Report the malaria status of this cell.
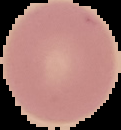

It is uninfected.

Summary:
  - Preparation: thin blood film
  - Image type: segmented cell region with the area outside set to black
  - Image size: 121×130 pixels